Identify the preparation type.
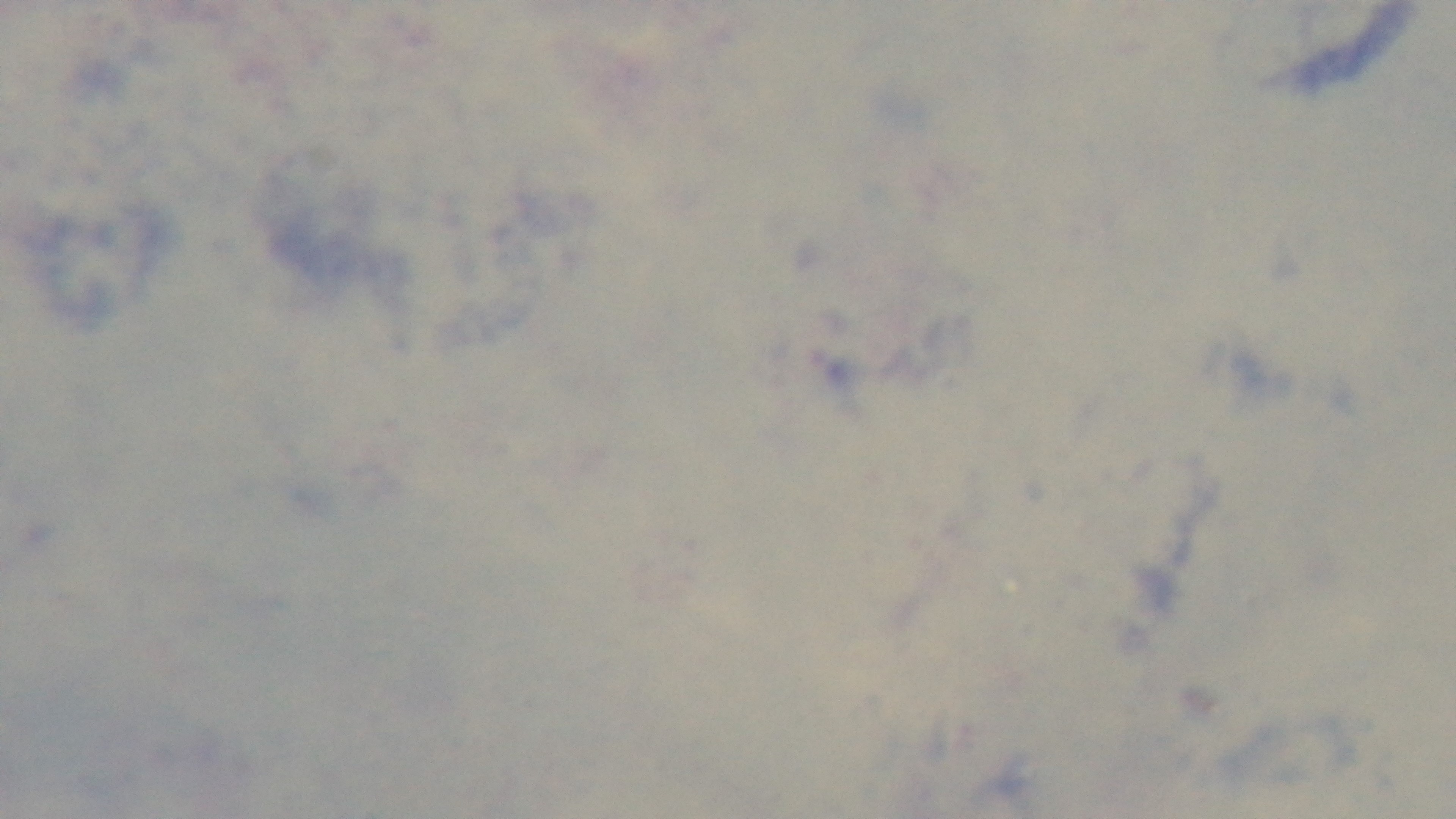

It is a thick blood film.

{
  "malaria_status": "uninfected",
  "modality": "light microscopy",
  "objective": "100x oil immersion",
  "field_of_view": "single",
  "capture": "mounted 4K digital camera",
  "stain": "Giemsa"
}